Outline each blood parasite and name the species.
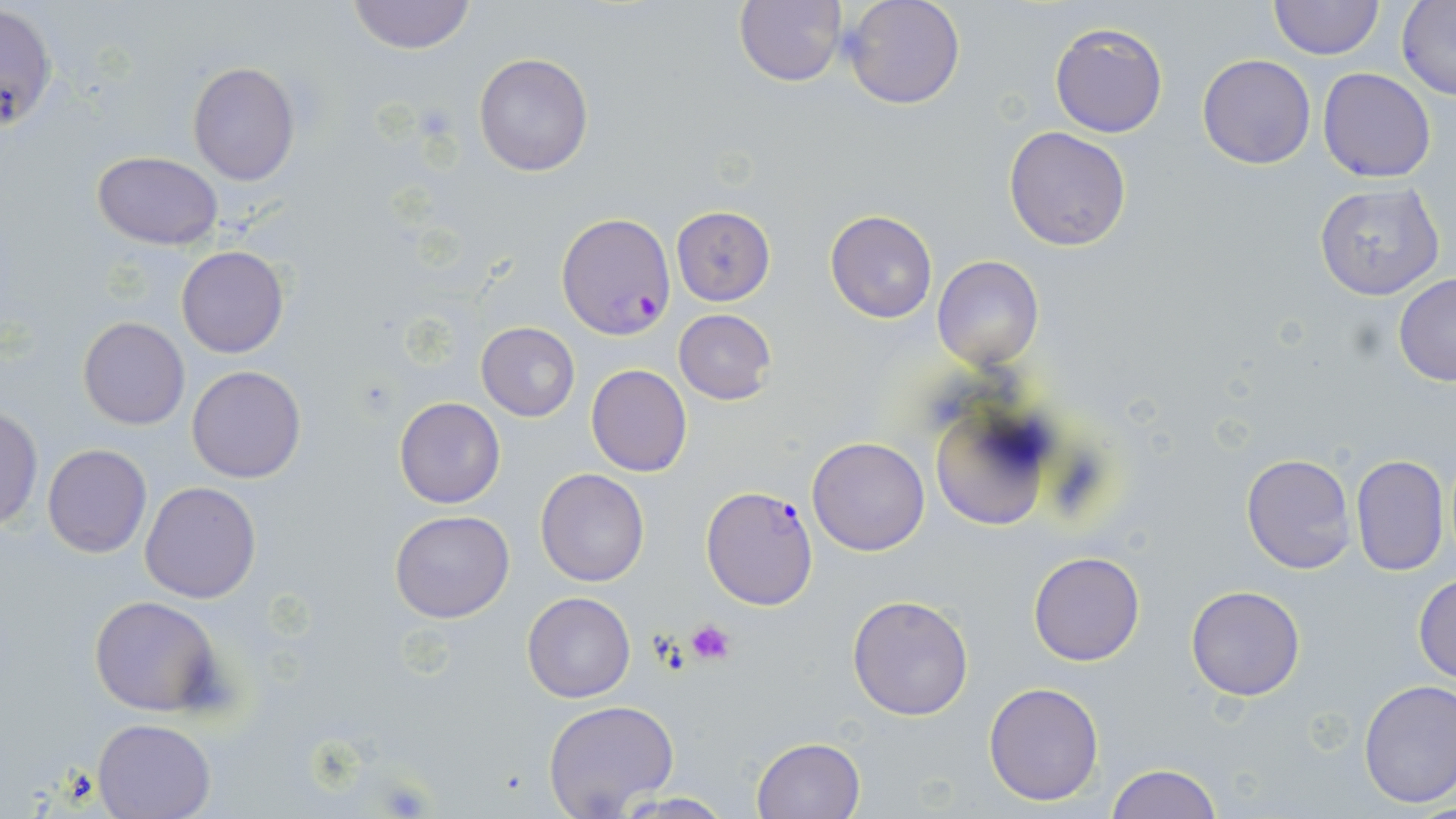

Approximate bounding boxes as (x1,y1)-(x2,y2) corner pairs in pixels.
Plasmodium falciparum-infected red blood cells: (1,4)-(59,134), (557,214)-(674,339), (702,484)-(819,610).
No Plasmodium ovale, Plasmodium malariae, Plasmodium vivax, Babesia divergens, or Trypanosoma brucei observed.

slide-level diagnosis = Plasmodium falciparum
modality = optical microscopy
platelet locations = approximate bounding boxes as (x1,y1)-(x2,y2) corner pairs in pixels: (687,619)-(735,666)
image size = 1456×819 pixels
uninfected red blood cell locations = approximate bounding boxes as (x1,y1)-(x2,y2) corner pairs in pixels: (346,0)-(475,55), (735,0)-(849,88), (841,0)-(966,110), (1269,0)-(1383,59), (1397,0)-(1455,100), (1050,23)-(1168,138), (474,53)-(594,176), (1197,54)-(1317,169), (187,61)-(300,185), (1318,67)-(1437,183), (1003,126)-(1132,251), (91,151)-(223,248), (1313,183)-(1445,301), (670,206)-(777,307), (825,210)-(938,324), (175,245)-(289,358), (932,255)-(1043,371), (1393,275)-(1456,386), (674,309)-(775,404), (77,316)-(190,431), (476,323)-(580,420), (586,364)-(692,477), (187,365)-(307,483), (928,396)-(1062,531), (394,397)-(506,509), (0,406)-(42,532), (807,436)-(931,555), (41,443)-(151,559), (1240,453)-(1356,575), (1349,454)-(1449,576), (536,468)-(649,586), (140,481)-(262,603), (389,510)-(514,624), (1028,551)-(1145,667), (1412,571)-(1456,685), (1185,585)-(1305,700), (521,592)-(636,702), (846,594)-(975,722), (89,595)-(223,716), (1357,679)-(1456,810), (983,681)-(1106,806), (542,700)-(680,819), (94,717)-(215,818), (752,736)-(867,819), (1106,764)-(1222,818), (608,792)-(740,818)
magnification = 1000x
stain = May-Grünwald-Giemsa
preparation = thin blood film
field of view = single